Assess the morphology of the erythrocytes.
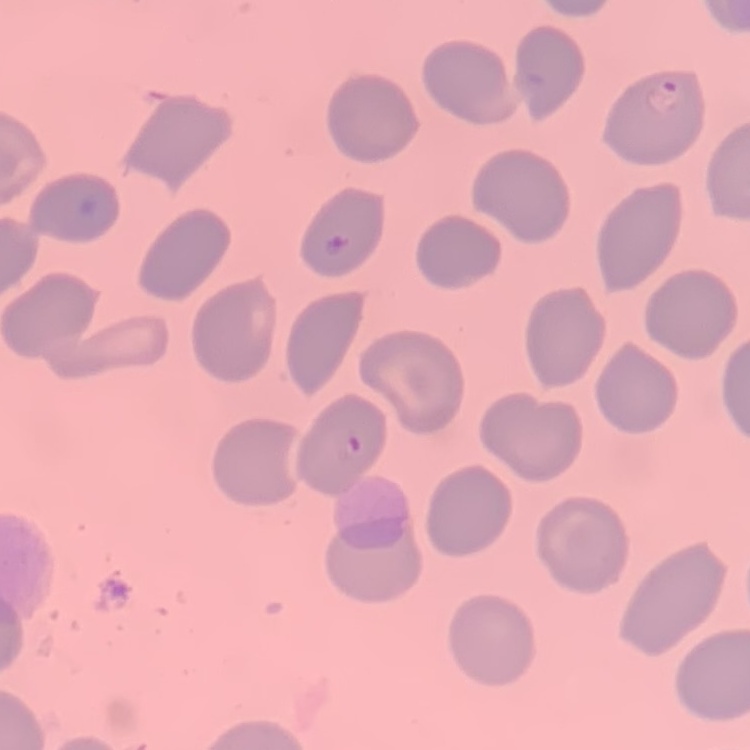
They show no rouleaux formation.

Summary:
  - Image type: square crop of a larger photomicrograph
  - Preparation: thin blood smear
  - Stain: Field's or Giemsa